Describe the morphology of the erythrocytes.
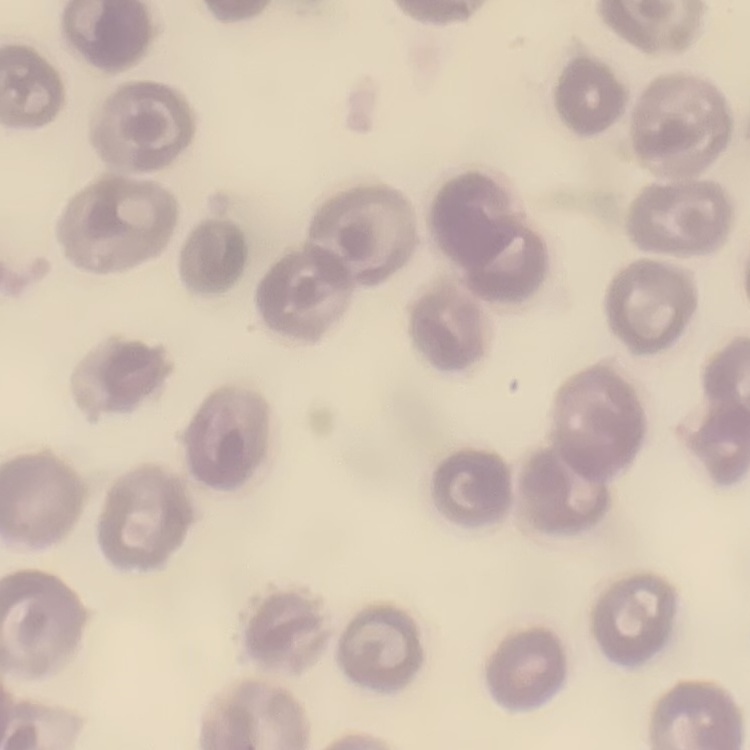
No rouleaux formation.

Summary:
  - Preparation: thin blood film
  - Stain: Field's or Giemsa
  - Image type: one tile cut from a larger photomicrograph